Point out each malaria parasite.
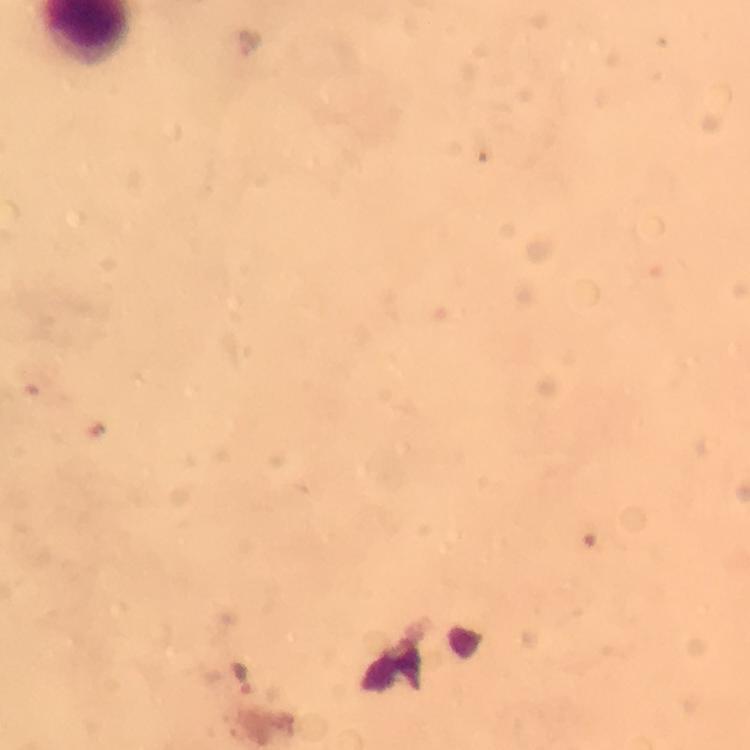

Approximate centers as [x, y] in pixels.
Malaria parasites: [251, 42].

Summary:
  - Image size: 750×750 pixels
  - Cropped from: one field of view
  - Magnification: 100x
  - Preparation: thick blood smear
  - Context: from a malaria diagnostic workup
  - Immersion oil: used
  - Capture: smartphone camera through the microscope
  - Stain: Giemsa